Assess for Plasmodium parasites.
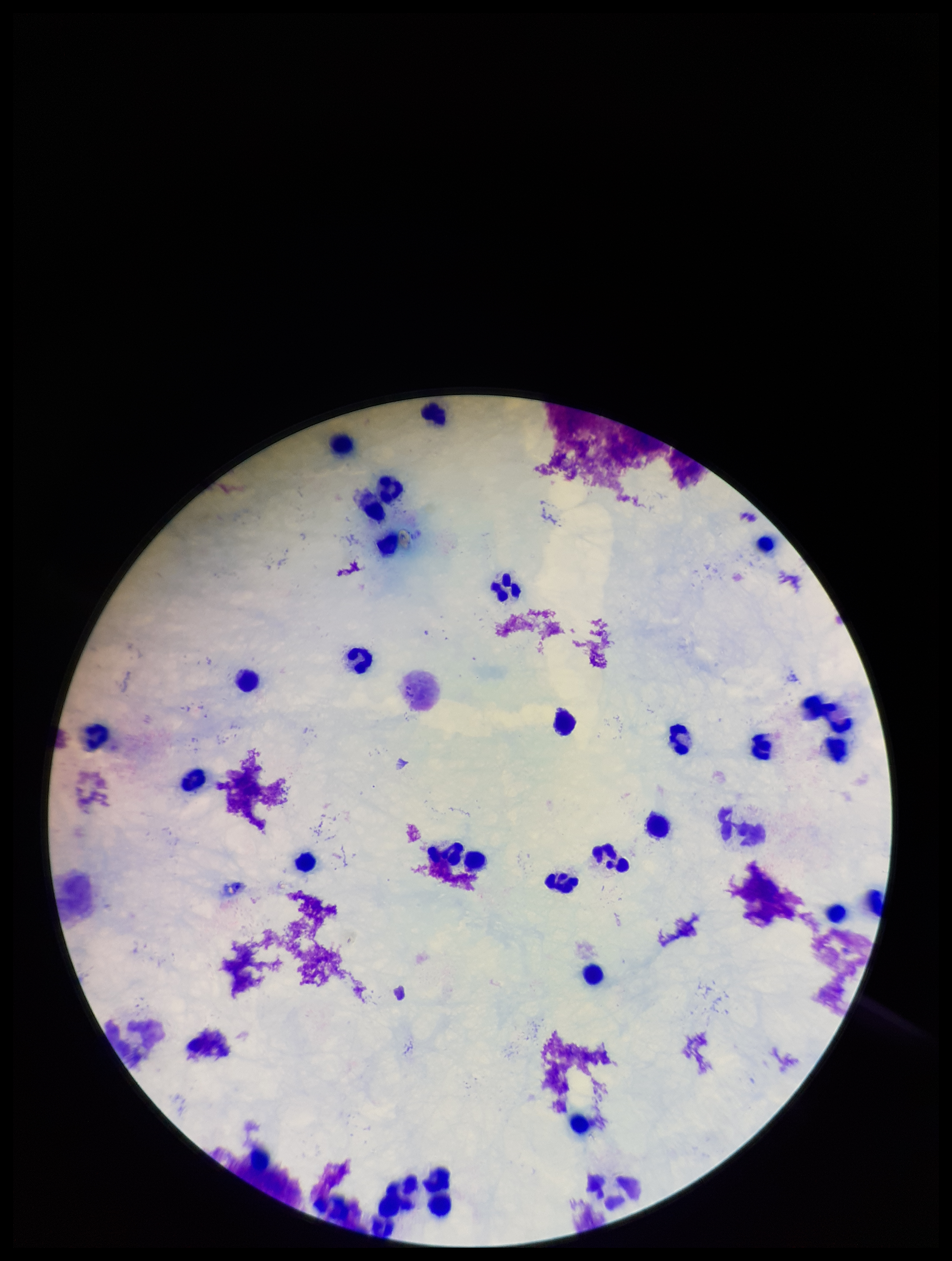

None detected.

Preparation: thick smear. Giemsa stain. Photographed through the microscope eyepiece with a smartphone camera. Image is 952×1261 pixels. Parasite count: 0. Patient malaria status: negative. Leukocyte count: 32. Single field of view.